Give the position of each Plasmodium falciparum parasite with its life-cycle stage, each leukocyte, and any debris.
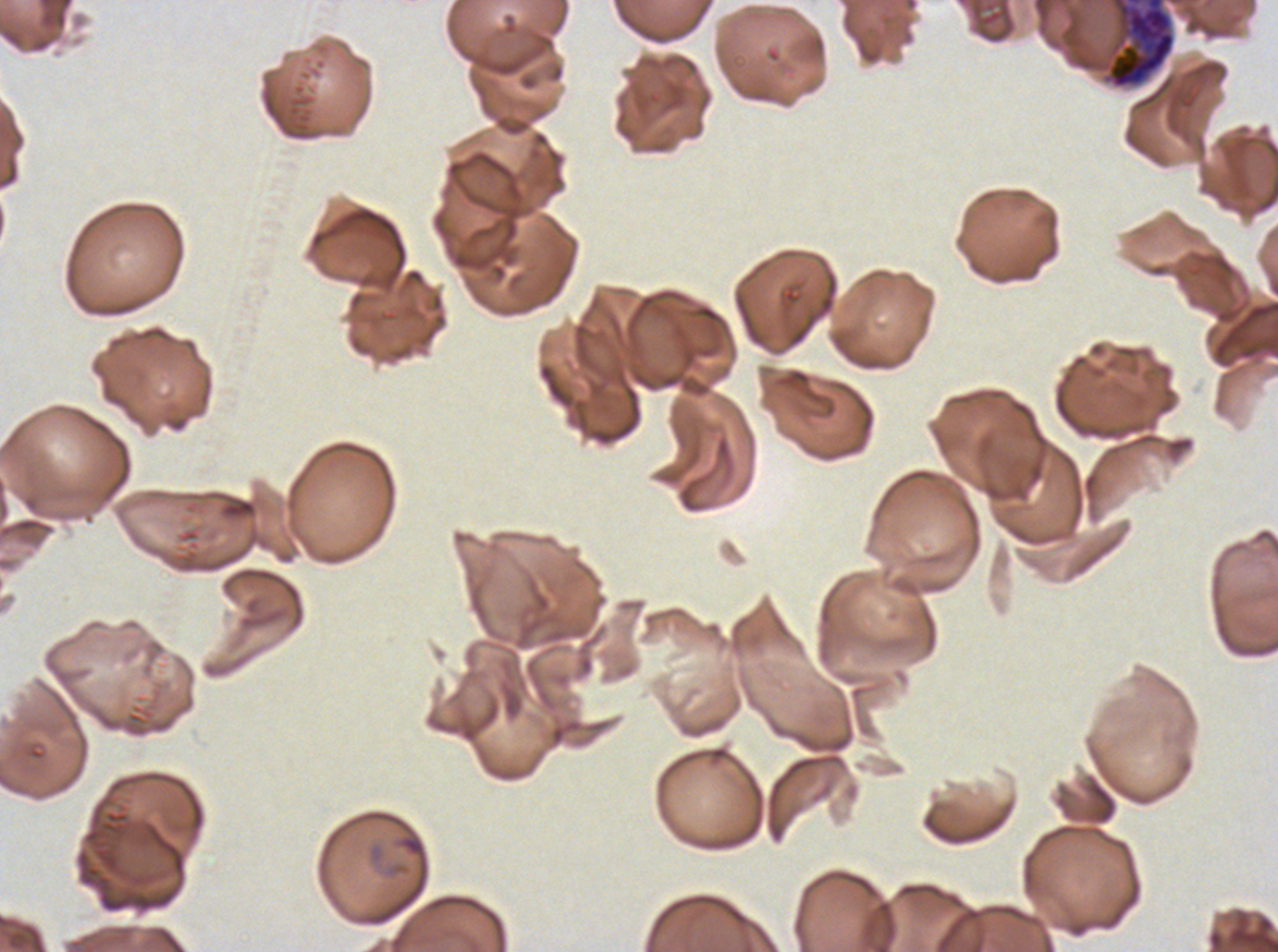

Approximate bounding boxes as [x1, y1, x2, y2] in pixels.
Early schizonts: [1101, 0, 1176, 90].
No rings, late-ring/early-trophozoite forms, mid trophozoites, late trophozoites, late schizonts, segmenters, gametocytes, leukocytes, or debris observed.

specimen = ex-vivo Plasmodium falciparum culture from a patient in The Gambia, grown for 24 to 48 hours
field of view = sub-image separated from a larger composite
preparation = thin blood film
image size = 1278×952 pixels
stain = Giemsa